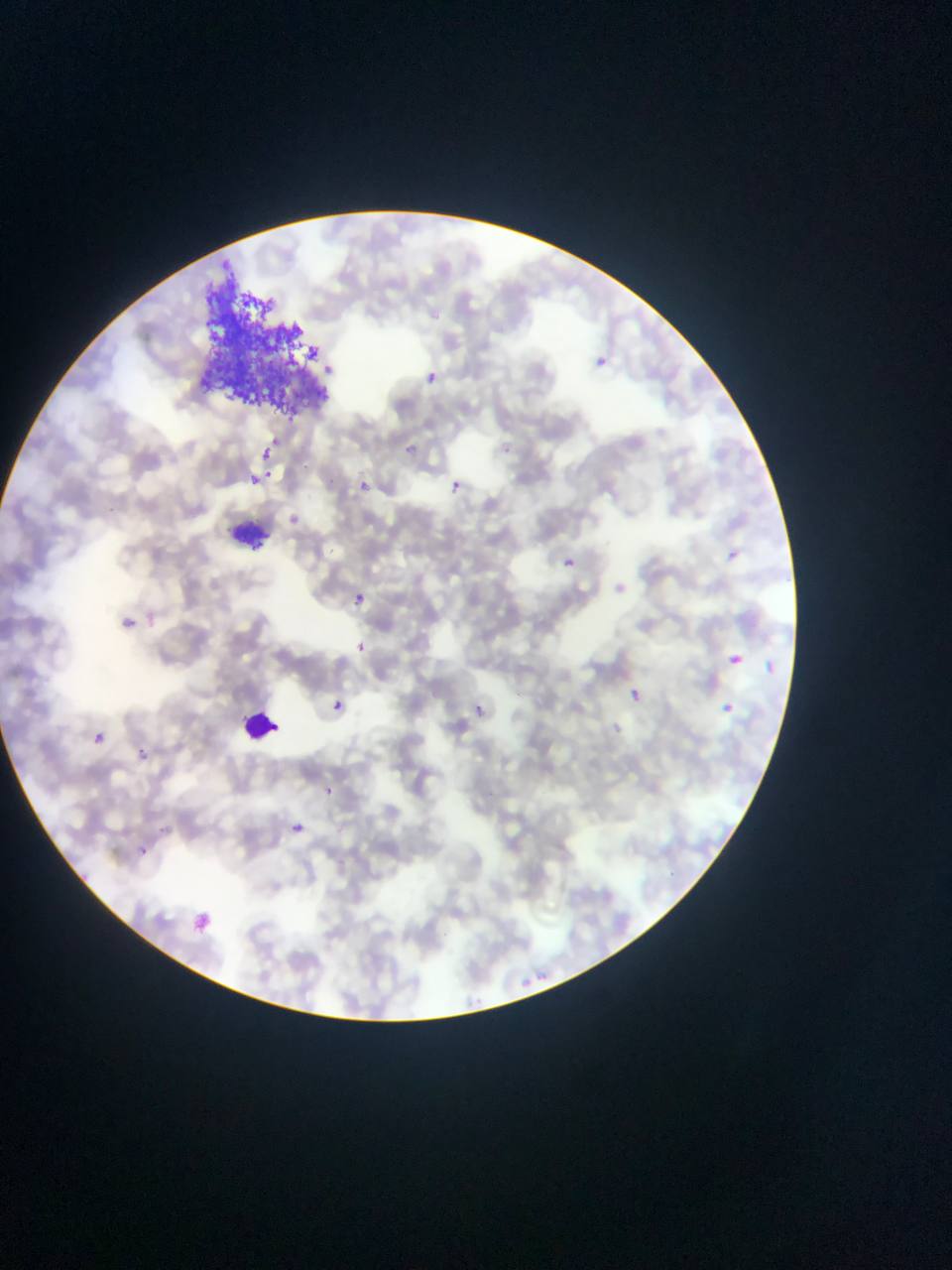

Approximate bounding boxes as (left, top, right, bottom) in pixels. Plasmodium parasite locations: (595, 355, 609, 368), (424, 369, 441, 385), (399, 441, 423, 459), (254, 443, 278, 473), (260, 447, 275, 462), (253, 468, 264, 487), (356, 478, 371, 492), (450, 478, 464, 492), (293, 511, 317, 531), (725, 548, 741, 563), (561, 555, 579, 570), (352, 589, 370, 608), (124, 617, 144, 636), (357, 637, 381, 661), (726, 652, 745, 667), (765, 660, 778, 675), (628, 687, 645, 704), (331, 697, 346, 712), (717, 699, 732, 715), (722, 702, 734, 713), (474, 704, 485, 714), (96, 727, 105, 742), (140, 747, 159, 770), (323, 781, 342, 805), (292, 816, 307, 835), (139, 844, 157, 859), (192, 912, 215, 937). Artifact (stain precipitate or debris) locations: (203, 271, 332, 434). Leukocyte locations: (239, 703, 280, 744). One field of view. Sample from Ghana. Image is 952×1270 pixels. Photographed through a microscope with a mobile-phone camera. Thin blood smear.